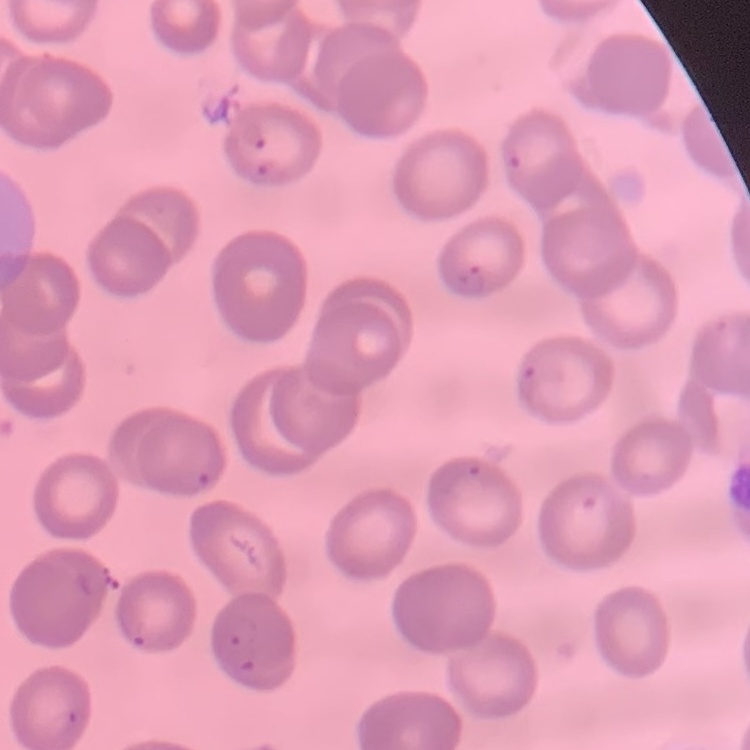 The erythrocytes exhibit no rouleaux formation. Square crop of a larger photomicrograph. Thin peripheral smear. Stained with either Field's or Giemsa.